Identify the cell.
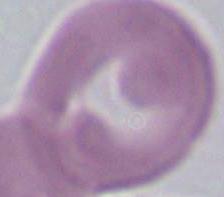

This is an erythrocyte.

Captured at 1000x magnification. Photomicrograph.